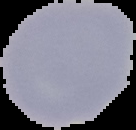
Image is 136×130 pixels. Segmented cell region on a black background. From a thin blood film. Result: no malaria parasites seen.